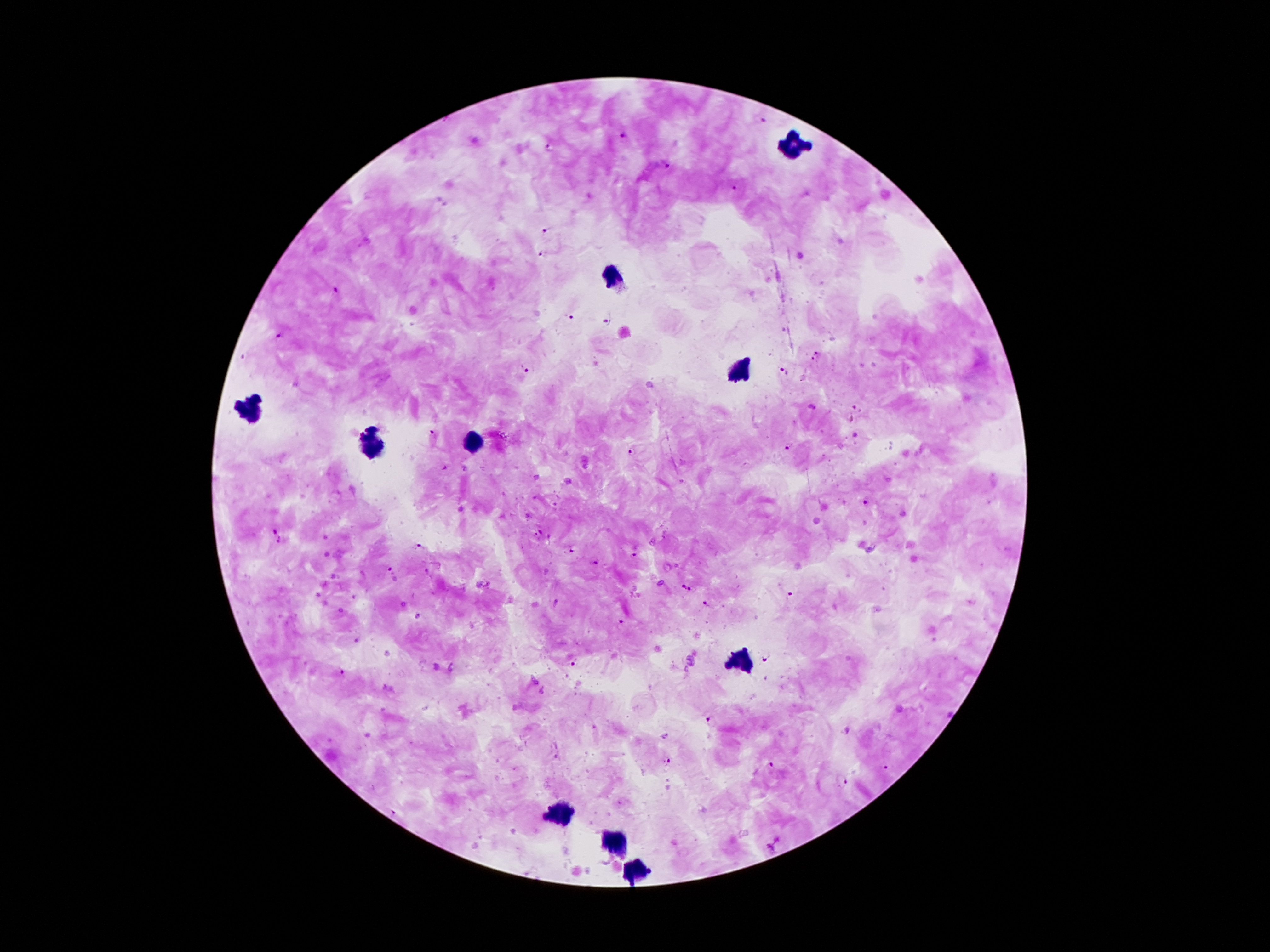

Approximate centers as {x, y} in pixels. Leukocyte locations: {791, 145}, {614, 276}, {739, 372}, {250, 413}, {477, 442}, {371, 444}, {742, 661}, {561, 815}, {614, 842}, {637, 868}. Plasmodium parasite locations: {761, 120}, {622, 135}, {549, 147}, {666, 167}, {735, 191}, {545, 231}, {540, 254}, {335, 291}, {570, 318}, {607, 321}, {279, 334}, {817, 353}, {243, 359}, {812, 360}, {526, 368}, {782, 372}, {856, 409}, {851, 420}, {432, 434}, {789, 447}, {633, 452}, {443, 469}, {866, 504}, {274, 530}, {538, 534}, {279, 541}, {418, 546}, {570, 550}, {634, 556}, {596, 560}, {390, 567}, {682, 585}, {692, 590}, {790, 597}, {556, 603}, {708, 606}, {621, 624}, {766, 658}, {573, 664}, {340, 673}, {711, 720}, {668, 761}, {772, 766}, {886, 769}, {841, 782}, {778, 840}, {769, 849}. Patient malaria status: positive for Plasmodium falciparum. Giemsa stain. 100x magnification. Image is 1270×952 pixels. Single field of view. Smartphone photograph taken through the microscope eyepiece. Thick peripheral-blood smear.